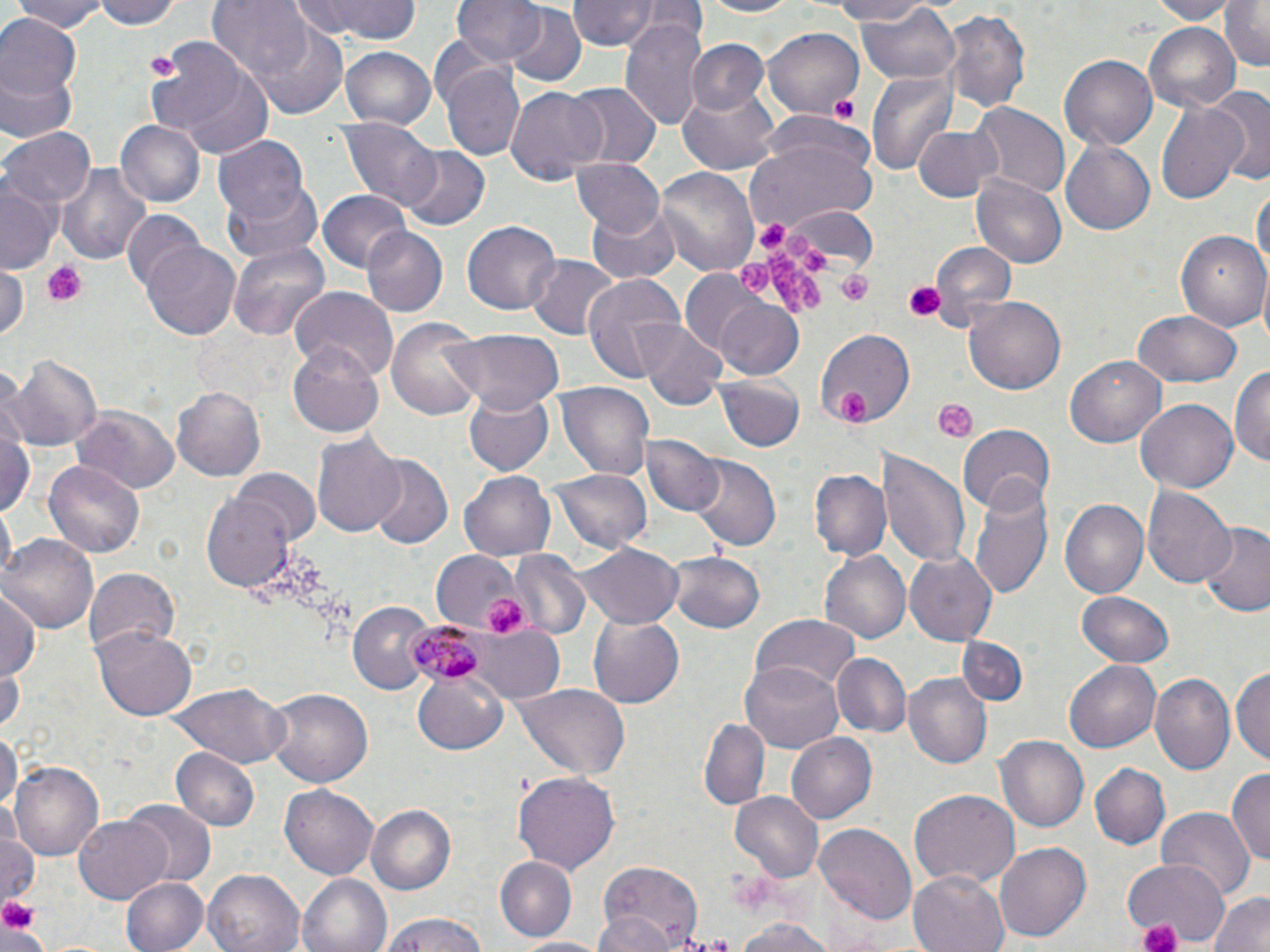
Summary:
  - Coordinate format: approximate bounding boxes as [x1, y1, x2, y2] in pixels
  - Plasmodium malariae-infected red blood cell locations: [402, 620, 493, 688]
  - Uninfected red blood cell locations: [9, 0, 108, 32], [90, 0, 186, 30], [208, 0, 316, 85], [291, 0, 423, 45], [454, 0, 545, 69], [566, 0, 675, 50], [697, 0, 805, 19], [823, 0, 934, 26], [1147, 0, 1235, 23], [1219, 0, 1270, 71], [856, 2, 961, 85], [504, 4, 588, 87], [942, 8, 1034, 113], [0, 16, 80, 102], [240, 19, 352, 118], [620, 19, 709, 132], [1143, 24, 1240, 110], [764, 28, 866, 117], [147, 36, 251, 138], [688, 40, 768, 117], [340, 46, 435, 130], [1060, 54, 1159, 152], [441, 56, 526, 162], [173, 58, 276, 160], [866, 67, 959, 177], [0, 69, 76, 144], [567, 82, 660, 167], [678, 83, 781, 174], [506, 86, 606, 183], [1211, 86, 1270, 185], [1154, 96, 1251, 210], [969, 102, 1069, 199], [340, 118, 440, 212], [116, 119, 208, 209], [912, 125, 1000, 204], [0, 126, 95, 212], [214, 138, 311, 227], [1059, 139, 1157, 237], [745, 140, 876, 231], [398, 144, 492, 230], [571, 157, 666, 237], [58, 161, 150, 268], [655, 166, 759, 276], [971, 174, 1067, 268], [222, 178, 324, 267], [0, 181, 58, 272], [1252, 182, 1269, 285], [318, 191, 414, 273], [587, 201, 682, 281], [785, 204, 879, 273], [121, 210, 206, 295], [462, 219, 561, 315], [360, 226, 447, 316], [1179, 228, 1270, 332], [142, 241, 243, 337], [227, 241, 329, 340], [931, 242, 1017, 324], [526, 254, 620, 342], [0, 264, 28, 339], [679, 268, 768, 355], [581, 274, 686, 386], [290, 287, 398, 383], [964, 295, 1069, 396], [714, 298, 804, 380], [1131, 311, 1242, 387], [387, 318, 486, 420], [636, 321, 728, 408], [814, 328, 917, 431], [442, 329, 566, 415], [289, 342, 386, 437], [6, 354, 103, 452], [1066, 354, 1166, 447], [1230, 366, 1270, 469], [713, 375, 804, 451], [554, 382, 654, 482], [172, 383, 267, 481], [463, 389, 554, 476], [1137, 398, 1240, 493], [71, 408, 181, 493], [1, 424, 35, 520], [955, 424, 1055, 512], [312, 432, 406, 538], [641, 435, 724, 518], [878, 445, 970, 570], [691, 456, 780, 552], [363, 457, 452, 548], [43, 458, 145, 558], [548, 465, 652, 557], [233, 469, 323, 546], [461, 469, 559, 562], [809, 469, 891, 564], [970, 480, 1052, 599], [1144, 485, 1235, 589], [201, 491, 298, 591], [1058, 498, 1149, 602], [1199, 523, 1269, 618], [2, 533, 98, 632], [573, 544, 682, 626], [669, 548, 765, 634], [430, 549, 523, 630], [818, 550, 910, 646], [904, 550, 1001, 647], [509, 552, 590, 641], [84, 567, 181, 656], [1076, 590, 1176, 668], [0, 591, 43, 682], [348, 602, 434, 693], [751, 614, 859, 694], [587, 615, 685, 708], [471, 628, 567, 704], [94, 629, 196, 720], [956, 637, 1029, 708], [833, 651, 909, 735], [1065, 659, 1161, 754], [740, 660, 845, 753], [1231, 662, 1269, 766], [0, 665, 25, 732], [1184, 668, 1269, 769], [412, 670, 509, 755], [903, 674, 988, 769], [1152, 674, 1235, 777], [513, 681, 632, 780], [165, 682, 290, 768], [265, 686, 374, 786], [699, 717, 770, 809], [0, 729, 19, 818], [786, 732, 876, 822], [995, 736, 1087, 833], [170, 747, 260, 832], [10, 761, 103, 861], [1091, 763, 1170, 848], [1229, 767, 1270, 871], [514, 771, 620, 872], [281, 784, 379, 880], [910, 790, 1018, 888], [731, 792, 822, 881], [123, 803, 214, 887], [366, 804, 458, 895], [1154, 806, 1255, 903], [73, 813, 171, 904], [814, 819, 916, 922], [1, 820, 39, 909], [995, 841, 1091, 944], [593, 856, 706, 948], [496, 857, 575, 940], [1124, 857, 1224, 945], [203, 869, 304, 952], [909, 871, 1010, 952], [297, 873, 393, 952], [120, 876, 208, 952], [1206, 893, 1270, 952], [375, 913, 492, 952], [595, 913, 676, 952], [735, 917, 833, 952], [513, 934, 608, 951]
  - Platelet locations: [145, 49, 182, 84], [826, 90, 860, 125], [753, 218, 785, 250], [782, 232, 809, 256], [801, 248, 829, 271], [769, 251, 823, 314], [44, 260, 88, 308], [737, 260, 771, 294], [838, 271, 875, 305], [904, 280, 946, 323], [836, 390, 871, 427], [933, 398, 979, 441], [485, 597, 527, 635], [0, 895, 41, 938], [1139, 920, 1181, 952]
  - Slide-level diagnosis: Plasmodium malariae
  - Preparation: thin blood smear
  - Modality: optical microscopy
  - Image size: 1270×952 pixels
  - Magnification: 1000x
  - Field of view: single
  - Stain: May-Grünwald-Giemsa